Outline each uninfected red blood cell.
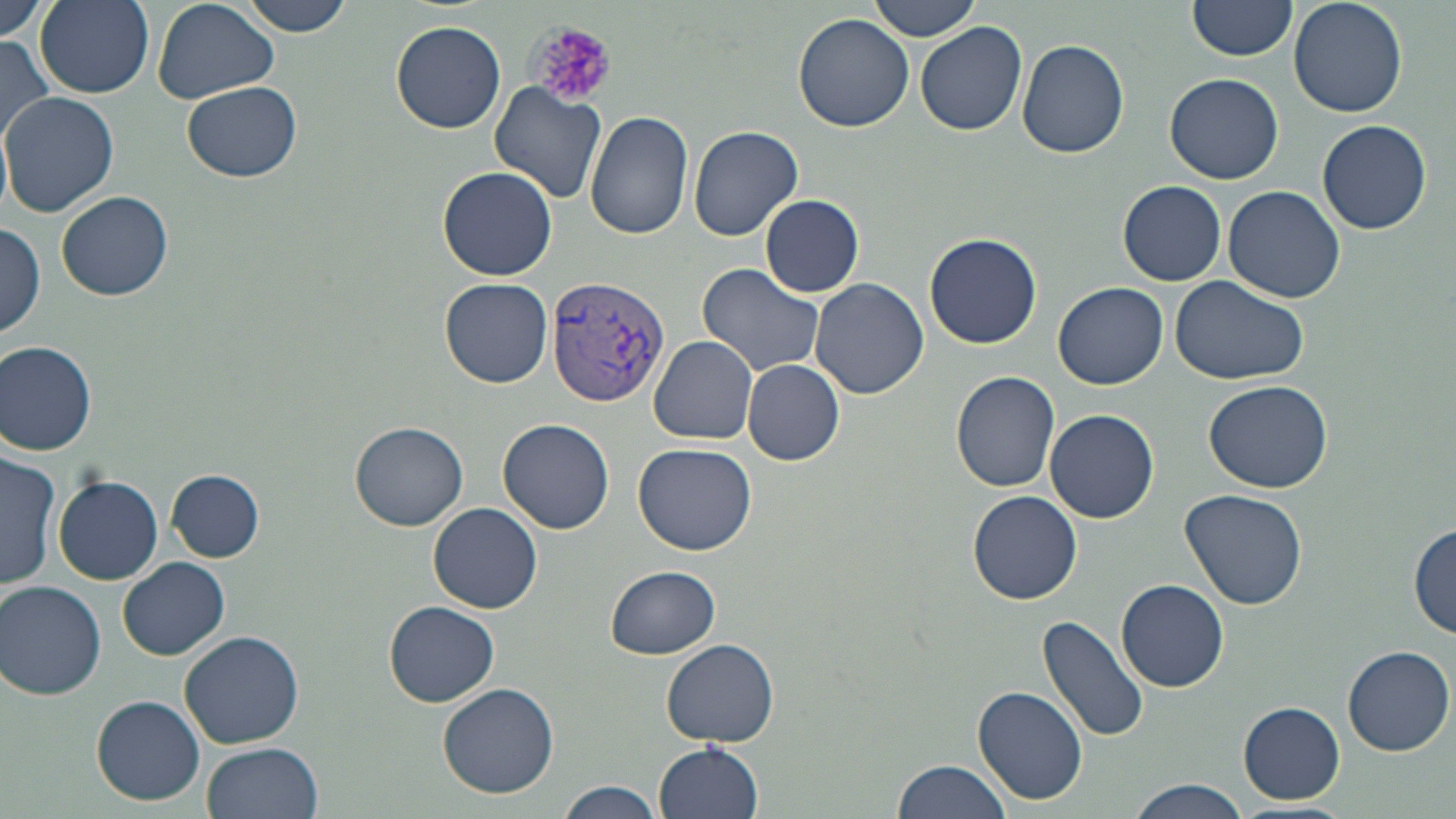
Approximate bounding boxes as named x1/y1/x2/y2 corners in pixels.
Uninfected red blood cells: (x1=0, y1=0, x2=51, y2=52), (x1=35, y1=0, x2=155, y2=97), (x1=235, y1=0, x2=358, y2=36), (x1=867, y1=0, x2=983, y2=40), (x1=1189, y1=0, x2=1299, y2=62), (x1=1288, y1=0, x2=1407, y2=118), (x1=150, y1=1, x2=278, y2=103), (x1=792, y1=12, x2=914, y2=134), (x1=390, y1=20, x2=506, y2=133), (x1=916, y1=22, x2=1028, y2=137), (x1=0, y1=36, x2=56, y2=149), (x1=1017, y1=38, x2=1130, y2=159), (x1=1166, y1=72, x2=1284, y2=184), (x1=184, y1=80, x2=301, y2=182), (x1=490, y1=84, x2=607, y2=204), (x1=2, y1=92, x2=119, y2=217), (x1=585, y1=110, x2=694, y2=240), (x1=1318, y1=119, x2=1432, y2=236), (x1=688, y1=124, x2=804, y2=242), (x1=438, y1=166, x2=558, y2=279), (x1=1117, y1=180, x2=1227, y2=285), (x1=1223, y1=185, x2=1346, y2=304), (x1=57, y1=190, x2=173, y2=301), (x1=760, y1=194, x2=865, y2=296), (x1=0, y1=221, x2=47, y2=339), (x1=923, y1=232, x2=1044, y2=350), (x1=698, y1=264, x2=825, y2=377), (x1=1168, y1=273, x2=1311, y2=386), (x1=809, y1=277, x2=928, y2=398), (x1=440, y1=278, x2=553, y2=387), (x1=1053, y1=283, x2=1168, y2=390), (x1=650, y1=335, x2=758, y2=444), (x1=0, y1=339, x2=100, y2=455), (x1=744, y1=359, x2=844, y2=466), (x1=950, y1=370, x2=1061, y2=493), (x1=1204, y1=379, x2=1332, y2=494), (x1=1046, y1=409, x2=1159, y2=524), (x1=497, y1=417, x2=615, y2=534), (x1=350, y1=422, x2=468, y2=529), (x1=633, y1=442, x2=757, y2=556), (x1=0, y1=449, x2=60, y2=590), (x1=167, y1=471, x2=263, y2=560), (x1=53, y1=476, x2=163, y2=584), (x1=1178, y1=488, x2=1310, y2=610), (x1=968, y1=491, x2=1082, y2=604), (x1=429, y1=503, x2=543, y2=613), (x1=1409, y1=522, x2=1456, y2=638), (x1=118, y1=557, x2=229, y2=659), (x1=604, y1=566, x2=721, y2=660), (x1=0, y1=580, x2=107, y2=700), (x1=1118, y1=580, x2=1229, y2=690), (x1=384, y1=600, x2=499, y2=707), (x1=1038, y1=614, x2=1150, y2=744), (x1=181, y1=630, x2=302, y2=748), (x1=662, y1=639, x2=779, y2=747), (x1=1343, y1=646, x2=1454, y2=756), (x1=438, y1=681, x2=560, y2=800), (x1=974, y1=686, x2=1088, y2=805), (x1=94, y1=695, x2=206, y2=805), (x1=1239, y1=701, x2=1346, y2=802), (x1=654, y1=741, x2=765, y2=819), (x1=202, y1=743, x2=323, y2=819), (x1=892, y1=758, x2=1015, y2=819), (x1=556, y1=780, x2=667, y2=819), (x1=1128, y1=780, x2=1250, y2=818).

Summary:
  - Plasmodium vivax-infected red blood cell locations: (x1=546, y1=276, x2=669, y2=407)
  - Platelet locations: (x1=526, y1=18, x2=618, y2=111)
  - Slide-level diagnosis: Plasmodium vivax
  - Preparation: thin blood film
  - Modality: light microscopy
  - Image size: 1456×819 pixels
  - Stain: May-Grünwald-Giemsa
  - Magnification: 1000x
  - Field of view: single